Identify the cell.
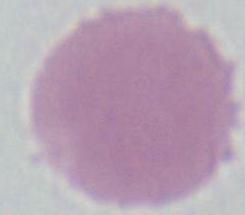
An erythrocyte.

Photomicrograph. 1000x magnification.